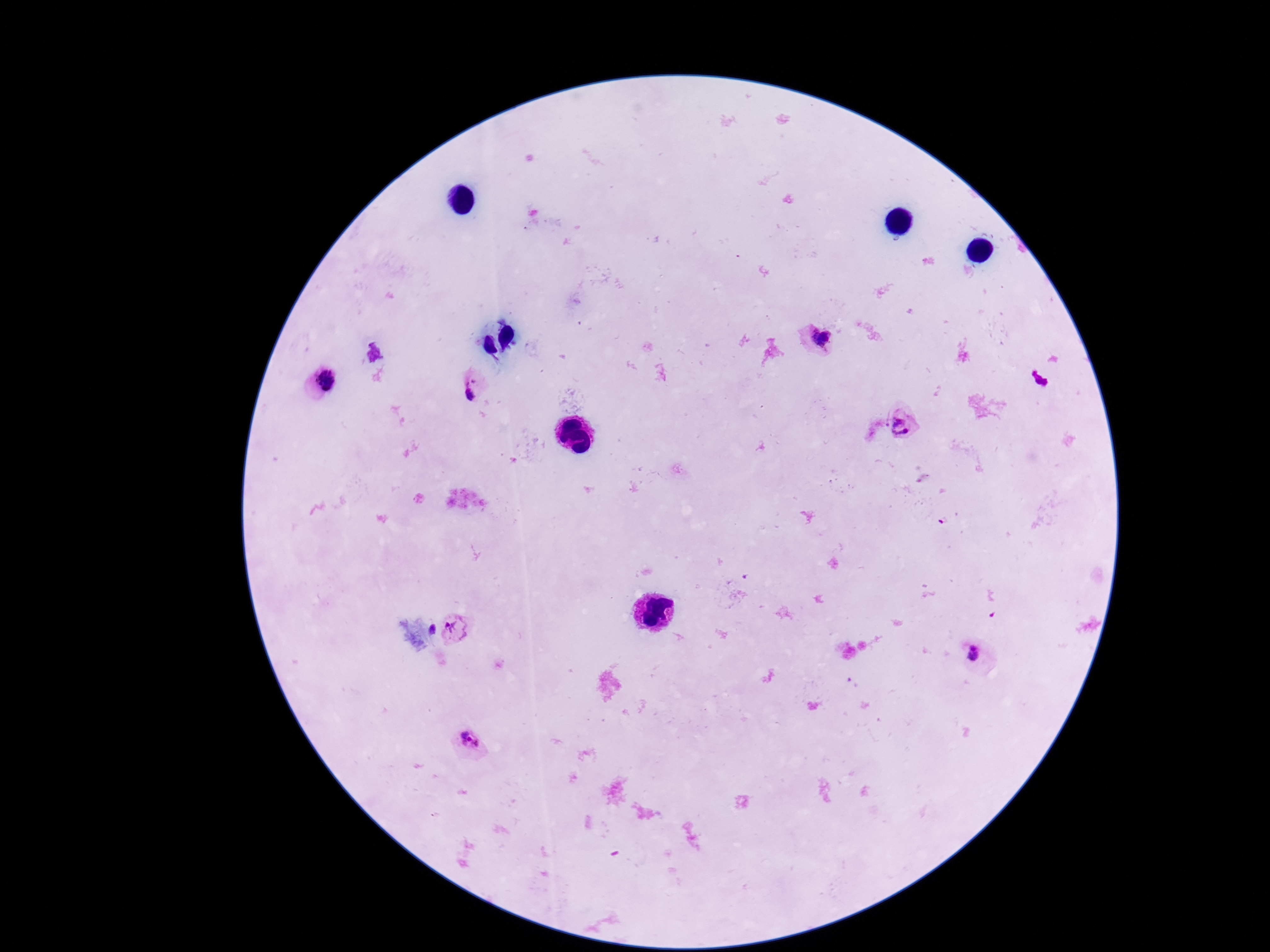

capture = smartphone camera through the microscope eyepiece
patient malaria status = infected
Plasmodium parasite locations = approximate centers as (x, y) in pixels: (817, 339), (1038, 379), (321, 380), (472, 386), (905, 423), (460, 631), (977, 659), (470, 743)
preparation = thick peripheral-blood smear
field of view = one from this slide
image size = 1270×952 pixels
stain = Giemsa
magnification = 100x